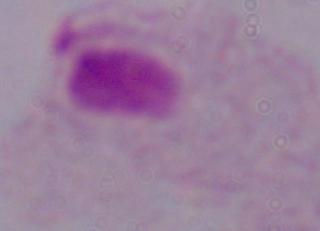 1000x magnification. Micrograph. A trichomonad is shown.